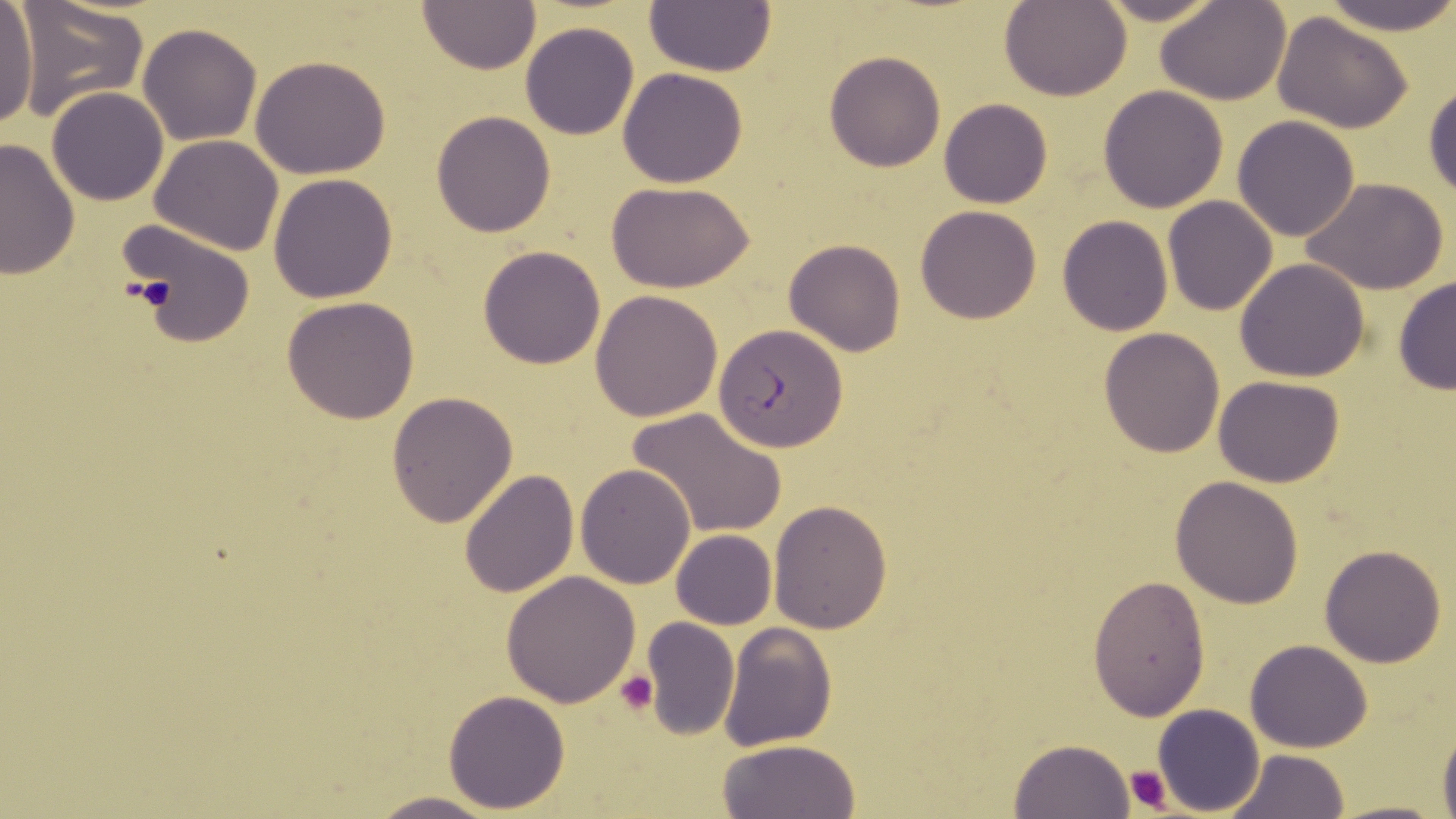
Summary:
  - Coordinate format: approximate bounding boxes as named x1/y1/x2/y2 corners in pixels
  - Plasmodium falciparum-infected red blood cell locations: (x1=715, y1=323, x2=846, y2=451)
  - Uninfected red blood cell locations: (x1=11, y1=0, x2=148, y2=122), (x1=1089, y1=0, x2=1228, y2=25), (x1=1156, y1=0, x2=1292, y2=104), (x1=1322, y1=0, x2=1455, y2=32), (x1=1001, y1=1, x2=1130, y2=101), (x1=416, y1=2, x2=542, y2=74), (x1=645, y1=2, x2=777, y2=76), (x1=0, y1=5, x2=38, y2=129), (x1=1272, y1=12, x2=1414, y2=133), (x1=519, y1=22, x2=640, y2=140), (x1=138, y1=23, x2=261, y2=146), (x1=825, y1=52, x2=944, y2=172), (x1=251, y1=54, x2=392, y2=179), (x1=617, y1=68, x2=749, y2=188), (x1=1425, y1=79, x2=1456, y2=202), (x1=1097, y1=85, x2=1229, y2=213), (x1=46, y1=87, x2=169, y2=207), (x1=939, y1=99, x2=1053, y2=209), (x1=430, y1=111, x2=557, y2=238), (x1=1232, y1=115, x2=1362, y2=242), (x1=149, y1=135, x2=286, y2=256), (x1=0, y1=137, x2=80, y2=280), (x1=268, y1=173, x2=399, y2=303), (x1=1301, y1=177, x2=1450, y2=295), (x1=608, y1=181, x2=754, y2=293), (x1=1163, y1=195, x2=1280, y2=316), (x1=915, y1=206, x2=1042, y2=325), (x1=1056, y1=215, x2=1174, y2=335), (x1=119, y1=221, x2=255, y2=346), (x1=783, y1=238, x2=907, y2=356), (x1=477, y1=245, x2=607, y2=369), (x1=1234, y1=258, x2=1370, y2=383), (x1=1392, y1=274, x2=1456, y2=397), (x1=589, y1=290, x2=724, y2=421), (x1=281, y1=297, x2=420, y2=423), (x1=1098, y1=326, x2=1226, y2=459), (x1=1213, y1=376, x2=1345, y2=488), (x1=386, y1=391, x2=517, y2=526), (x1=630, y1=408, x2=786, y2=539), (x1=575, y1=463, x2=697, y2=588), (x1=458, y1=468, x2=579, y2=597), (x1=1171, y1=475, x2=1304, y2=608), (x1=768, y1=500, x2=892, y2=634), (x1=670, y1=530, x2=777, y2=629), (x1=1318, y1=543, x2=1448, y2=667), (x1=501, y1=571, x2=640, y2=707), (x1=1087, y1=575, x2=1210, y2=718), (x1=641, y1=617, x2=740, y2=740), (x1=716, y1=622, x2=836, y2=753), (x1=1244, y1=639, x2=1372, y2=753), (x1=442, y1=689, x2=570, y2=812), (x1=1152, y1=704, x2=1265, y2=815), (x1=1437, y1=719, x2=1456, y2=819), (x1=719, y1=738, x2=861, y2=819), (x1=1009, y1=739, x2=1135, y2=819), (x1=1227, y1=749, x2=1348, y2=819), (x1=365, y1=791, x2=499, y2=819), (x1=1328, y1=799, x2=1447, y2=819)
  - Platelet locations: (x1=130, y1=273, x2=179, y2=312), (x1=615, y1=671, x2=657, y2=715), (x1=1123, y1=764, x2=1175, y2=814)
  - Slide-level diagnosis: Plasmodium falciparum
  - Modality: optical microscopy
  - Stain: May-Grünwald-Giemsa
  - Magnification: 1000x
  - Image size: 1456×819 pixels
  - Preparation: thin blood film
  - Field of view: one of a larger specimen